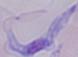

{
  "magnification": "1000x",
  "modality": "micrograph",
  "identification": "trypanosome"
}